Name the blood parasite species.
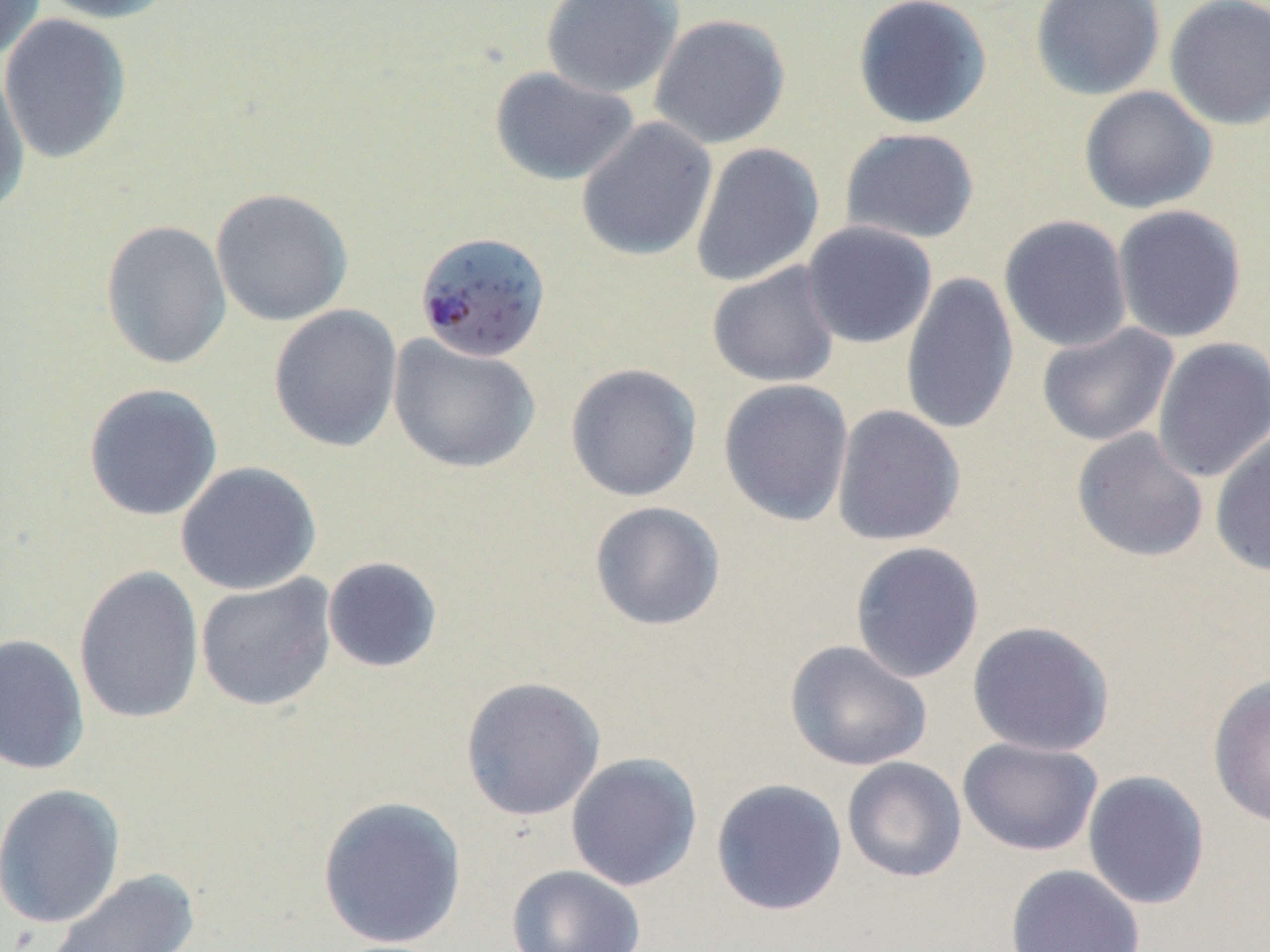

Plasmodium falciparum.

{
  "field_of_view": "one of a larger specimen",
  "plasmodium_falciparum_infected_red_blood_cell_locations": "approximate bounding boxes as [x1, y1, x2, y2] in pixels: [418, 233, 557, 367]",
  "image_size": "1270×952 pixels",
  "magnification": "1000x",
  "uninfected_red_blood_cell_locations": "approximate bounding boxes as [x1, y1, x2, y2] in pixels: [0, 0, 47, 63], [34, 0, 179, 24], [540, 0, 683, 99], [853, 0, 993, 130], [1029, 0, 1166, 101], [1163, 0, 1270, 131], [0, 14, 133, 164], [649, 14, 791, 149], [0, 60, 31, 217], [489, 66, 639, 187], [1078, 85, 1218, 214], [576, 118, 718, 262], [839, 127, 980, 245], [690, 143, 825, 287], [210, 187, 353, 327], [1112, 204, 1247, 343], [999, 215, 1133, 352], [100, 220, 232, 370], [801, 221, 937, 349], [706, 261, 841, 388], [900, 271, 1019, 437], [268, 304, 403, 452], [1036, 323, 1179, 446], [388, 334, 541, 475], [1152, 337, 1270, 483], [565, 363, 702, 502], [718, 379, 854, 527], [83, 383, 224, 521], [831, 405, 966, 547], [1071, 428, 1209, 563], [1209, 431, 1270, 578], [175, 461, 321, 596], [588, 501, 726, 631], [850, 541, 985, 683], [321, 556, 444, 674], [73, 565, 205, 725], [195, 574, 338, 712], [967, 621, 1115, 756], [0, 633, 90, 775], [784, 640, 934, 772], [1207, 674, 1270, 828], [459, 676, 606, 821], [957, 737, 1103, 856], [565, 752, 703, 891], [841, 756, 967, 883], [1082, 770, 1211, 910], [710, 778, 848, 917], [0, 783, 126, 928], [316, 795, 467, 949], [1006, 863, 1145, 952], [506, 864, 646, 952], [46, 869, 201, 951]",
  "modality": "light microscopy",
  "stain": "May-Grünwald-Giemsa",
  "preparation": "thin blood film"
}